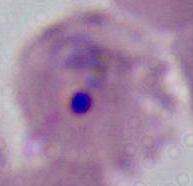
magnification = 400x or 1000x
identification = Plasmodium
modality = micrograph